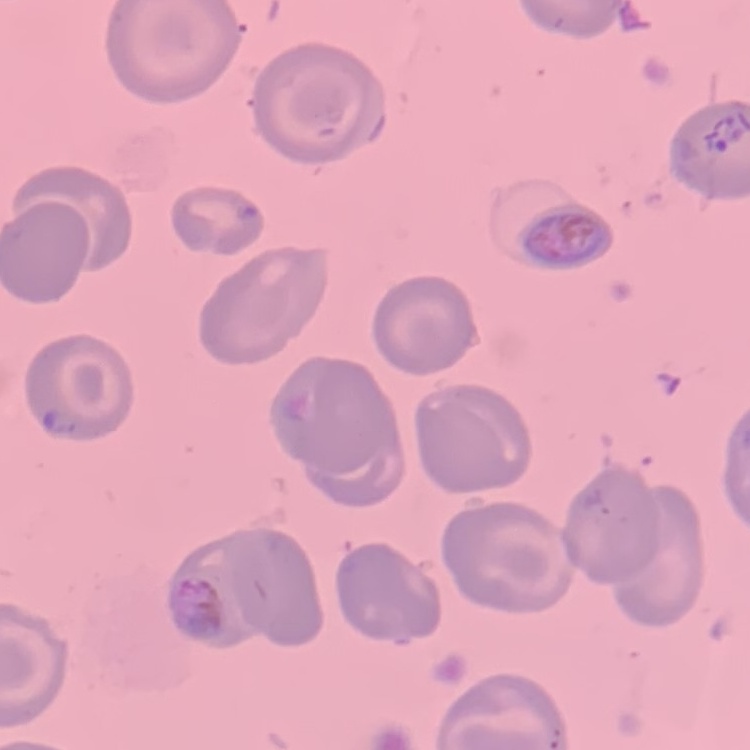 The erythrocytes show no rouleaux formation. Field's or Giemsa stain. Square crop of a larger photomicrograph. Thin peripheral smear.